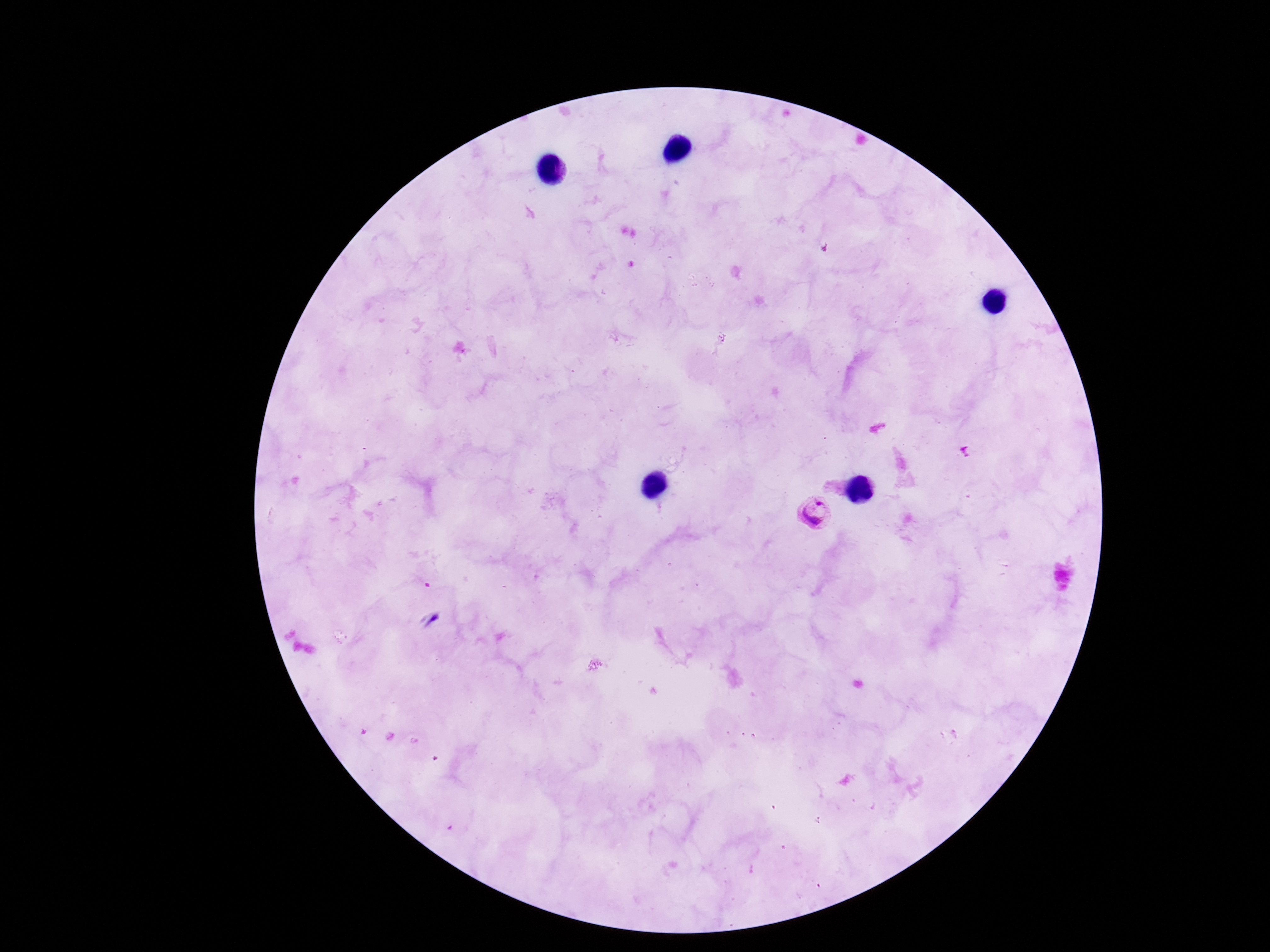

Approximate object centers, in pixels from the top-left corner. Plasmodium parasite locations: (x=815, y=513). Giemsa-stained preparation. Photographed through the microscope eyepiece with a smartphone camera. 100x magnification. Thick peripheral-blood smear. Single field of view. Patient malaria status: positive. Image is 1270×952 pixels.